Locate every Plasmodium parasite by life-cycle stage, and every leukocyte.
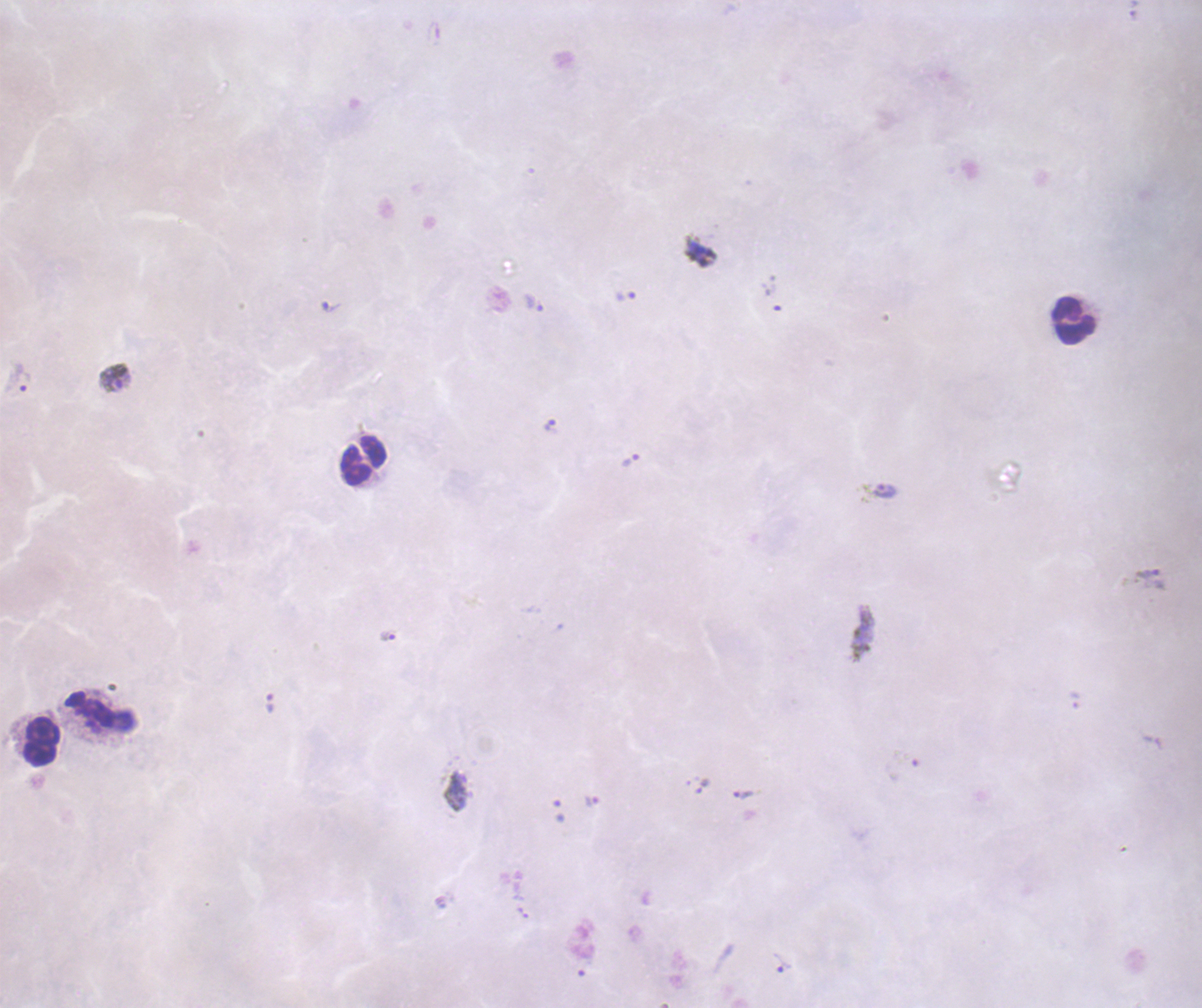
Approximate centers as (x, y) in pixels.
Trophozoites: (625, 296), (533, 303), (115, 377), (551, 427), (631, 459), (886, 491), (1151, 579), (388, 635), (270, 703), (743, 795), (591, 801), (781, 963).
No schizont or gametocyte forms observed.
Leukocytes: (1073, 320), (364, 461), (90, 710), (40, 743).

Thick smear of blood. Captured at 100x magnification. Image is 1202×1008 pixels. Coloration quality: bad. Previously used in an actual diagnosis. Romanowsky-stained preparation. Background quality: poor. Single field of view.